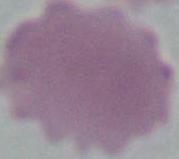 An erythrocyte is seen. 1000x magnification. Micrograph.